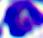
magnification = 400x
identification = leukocyte
modality = micrograph